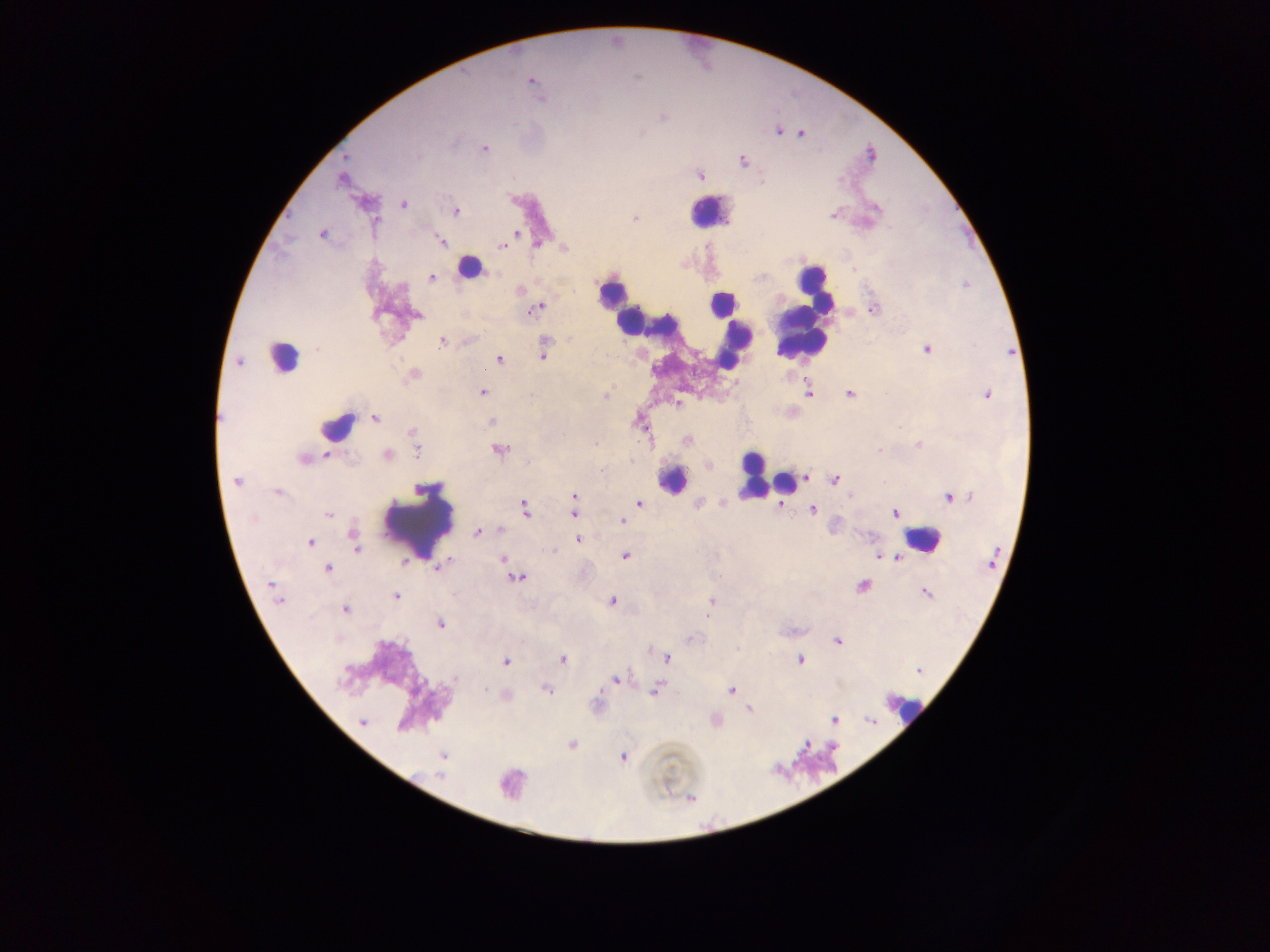

{
  "plasmodium_parasite_locations": "approximate centers as (x, y) in pixels: (531, 80), (662, 117), (779, 132), (801, 133), (484, 148), (743, 160), (700, 176), (341, 180), (403, 205), (456, 212), (833, 215), (636, 218), (322, 234), (516, 234), (440, 241), (537, 244), (502, 246), (564, 248), (431, 278), (538, 308), (873, 310), (417, 315), (441, 342), (927, 350), (543, 356), (499, 358), (239, 363), (413, 374), (482, 393), (808, 393), (849, 394), (987, 394), (606, 397), (677, 403), (376, 418), (492, 421), (336, 427), (414, 435), (687, 439), (595, 443), (919, 445), (415, 448), (500, 450), (387, 455), (304, 459), (601, 470), (806, 478), (835, 480), (237, 482), (277, 492), (575, 496), (952, 497), (639, 503), (780, 506), (525, 508), (813, 509), (574, 513), (327, 514), (896, 514), (623, 522), (500, 529), (477, 533), (579, 540), (310, 542), (356, 542), (879, 555), (624, 556), (896, 557), (504, 558), (405, 562), (439, 566), (509, 568), (328, 569), (517, 578), (863, 586), (926, 593), (397, 595), (280, 601), (612, 601), (712, 602), (345, 609), (440, 624), (837, 641), (667, 658), (563, 659), (800, 659), (505, 661), (919, 671), (455, 679), (616, 679), (546, 690), (656, 691), (732, 691), (749, 710), (834, 720), (362, 722), (572, 745), (442, 755), (623, 757), (440, 775)",
  "objects_each_labeled_both_plasmodium_parasite_and_leukocyte_by_the_source": "approximate centers as (x, y) in pixels: (470, 268), (672, 479), (786, 483)",
  "preparation": "thick blood film",
  "country": "Ghana",
  "capture": "mobile-phone photograph through a microscope",
  "leukocyte_locations": "approximate centers as (x, y) in pixels: (707, 211), (611, 293), (811, 302), (720, 304), (630, 321), (803, 328), (732, 337), (282, 357), (753, 476), (418, 523), (917, 539), (905, 709)",
  "field_of_view": "single",
  "image_size": "1270×952 pixels"
}